Locate and identify every blood parasite.
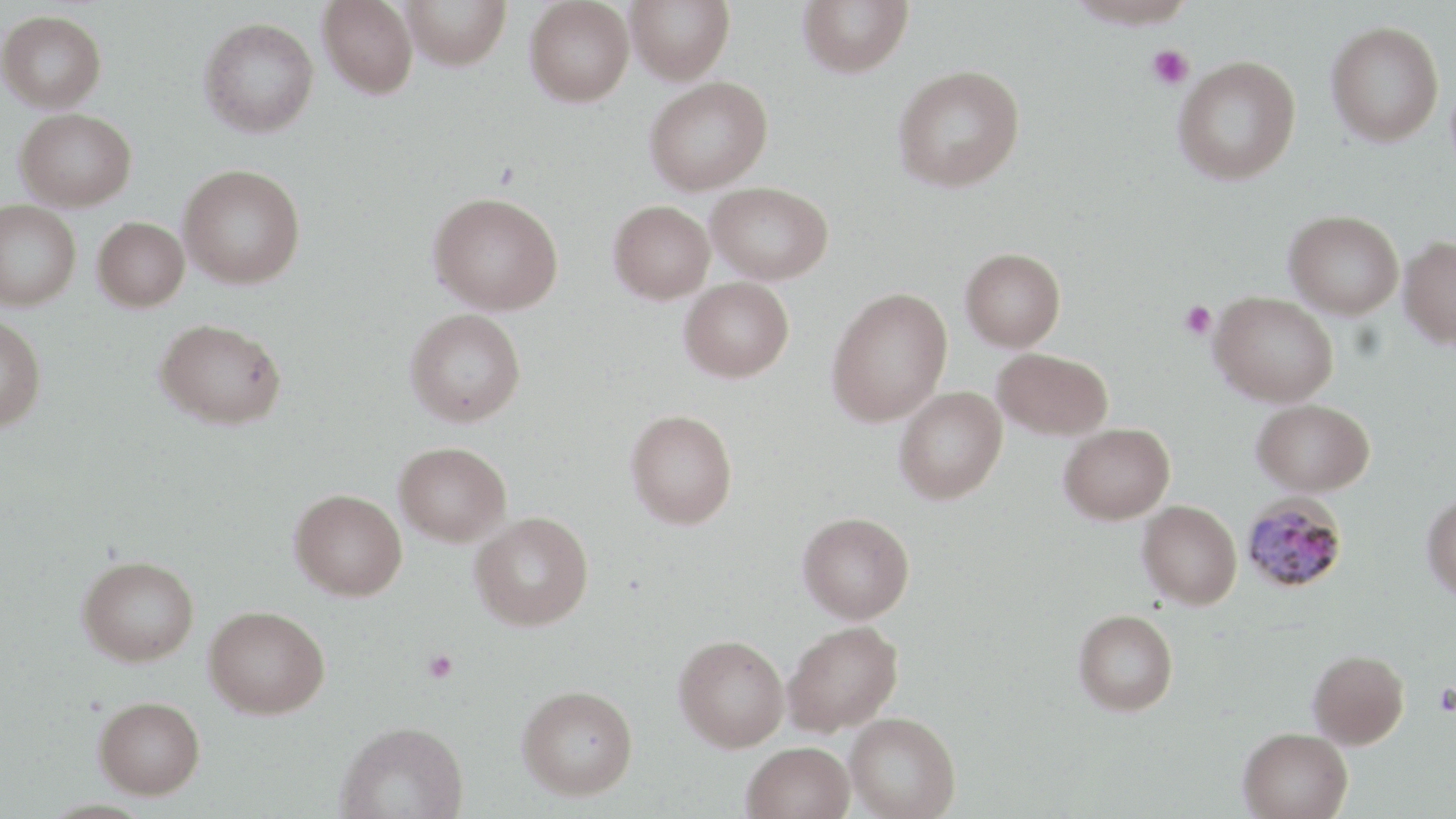
Approximate bounding boxes as (x1, y1, x2, y2) in pixels.
Plasmodium malariae-infected red blood cells: (1241, 492, 1349, 594).
No Plasmodium falciparum, Plasmodium ovale, Plasmodium vivax, Babesia divergens, or Trypanosoma brucei observed.

slide_level_diagnosis: Plasmodium malariae
modality: optical microscopy
magnification: 1000x
field_of_view: single
stain: May-Grünwald-Giemsa
uninfected_red_blood_cell_locations: 'approximate bounding boxes as (x1, y1, x2, y2) in pixels: (317, 0, 418, 98), (401, 0, 511, 70), (626, 0, 734, 84), (798, 0, 913, 77), (1066, 0, 1199, 27), (524, 1, 634, 107), (0, 10, 107, 112), (199, 17, 319, 138), (1326, 20, 1444, 146), (1173, 55, 1301, 184), (891, 64, 1025, 192), (644, 76, 773, 195), (14, 108, 136, 211), (178, 164, 306, 289), (706, 181, 833, 284), (428, 191, 564, 315), (0, 200, 81, 310), (608, 200, 715, 304), (1283, 210, 1404, 319), (93, 216, 189, 312), (1398, 236, 1456, 348), (960, 248, 1066, 351), (679, 277, 794, 382), (826, 286, 953, 427), (1209, 291, 1338, 406), (405, 309, 526, 427), (0, 315, 47, 431), (155, 318, 287, 429), (992, 347, 1114, 440), (893, 387, 1008, 504), (1252, 398, 1375, 496), (626, 409, 738, 528), (1058, 424, 1175, 524), (394, 441, 512, 545), (290, 488, 407, 601), (1422, 492, 1456, 603), (1138, 500, 1242, 610), (470, 511, 594, 631), (797, 511, 915, 623), (77, 554, 199, 666), (203, 605, 330, 718), (1073, 609, 1178, 716), (783, 620, 903, 735), (674, 634, 789, 752), (1308, 649, 1409, 749), (517, 685, 638, 799), (94, 695, 205, 798), (845, 711, 961, 819), (337, 720, 468, 819), (1238, 727, 1353, 819), (742, 741, 855, 819)'
preparation: thin blood smear
platelet_locations: 'approximate bounding boxes as (x1, y1, x2, y2) in pixels: (1146, 44, 1193, 90), (1179, 300, 1217, 340), (421, 649, 459, 683), (1435, 683, 1456, 716)'
image_size: 1456×819 pixels